Describe the morphology of the erythrocytes.
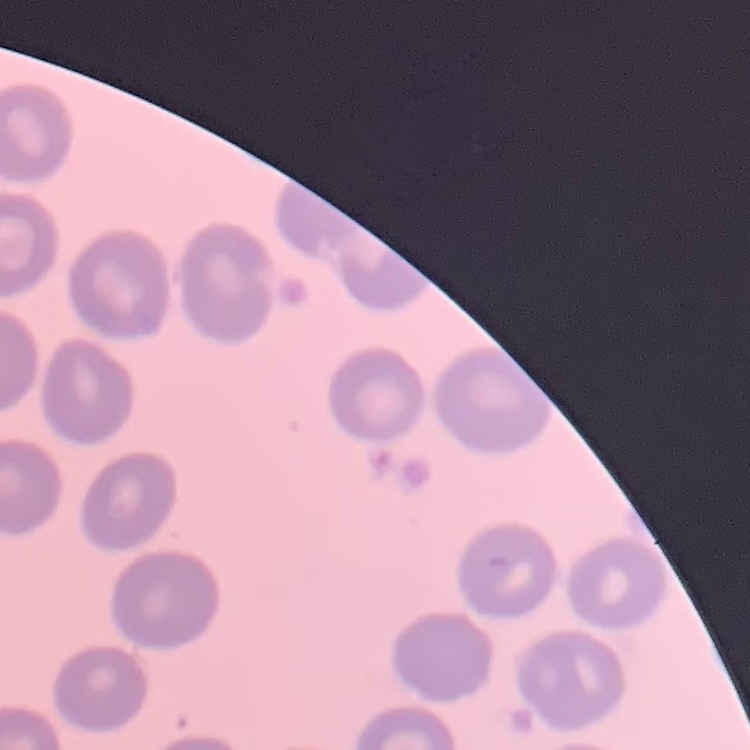
No rouleaux formation.

{
  "stain": "Field's or Giemsa",
  "image_type": "one tile cut from a larger photomicrograph",
  "preparation": "thin peripheral smear"
}